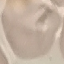 Result: no malaria parasites seen. Thin blood film. Automatically extracted cell patch, resized to 64 × 64 pixels. Giemsa-stained preparation. Acquired by smartphone through the microscope eyepiece.